Give the extent of all uninfected red blood cells.
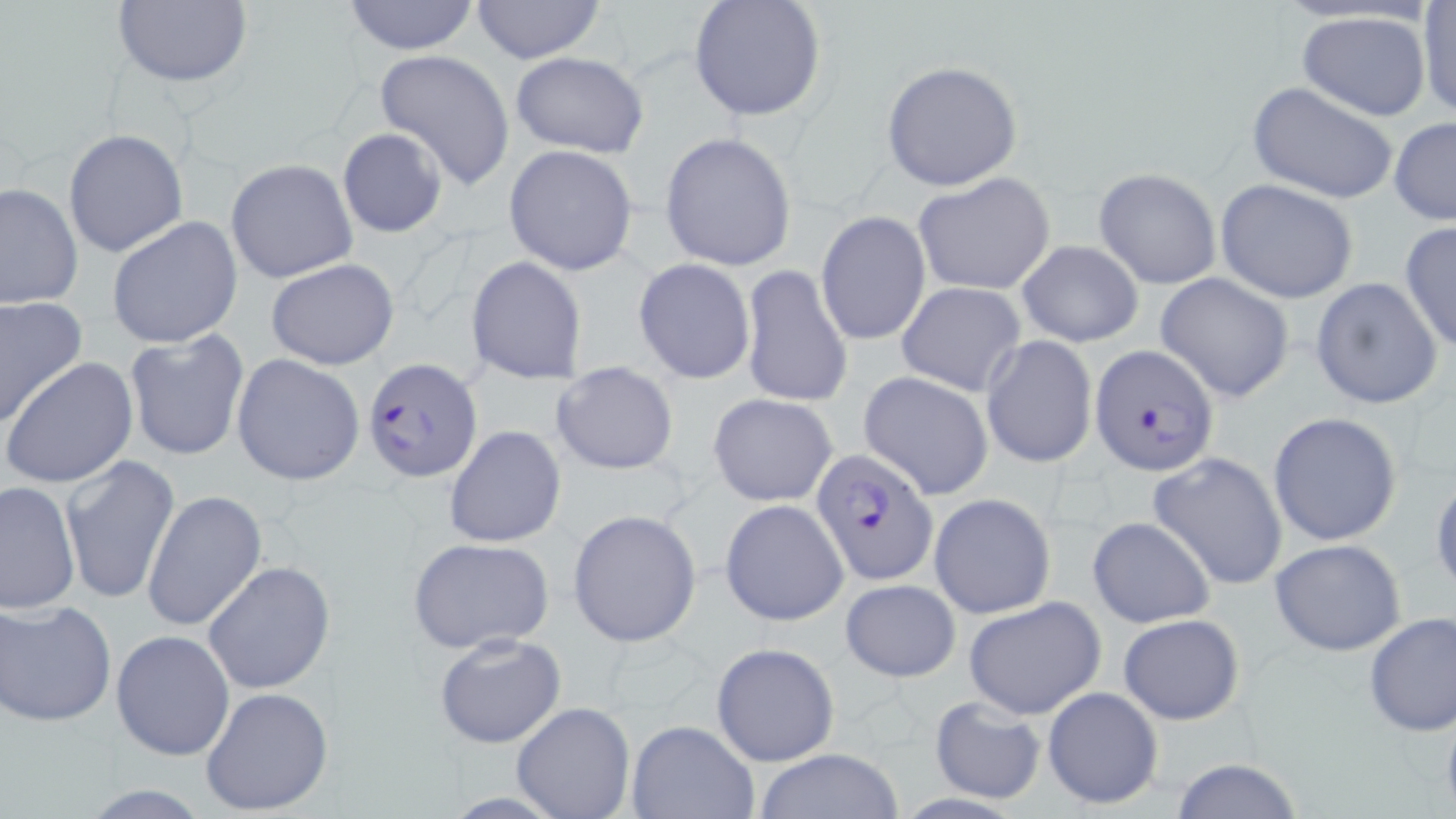
Approximate bounding boxes as (x1, y1, x2, y2) in pixels.
Uninfected red blood cells: (110, 0, 252, 91), (340, 0, 481, 55), (468, 0, 606, 65), (688, 0, 826, 123), (1416, 2, 1455, 120), (1297, 10, 1433, 121), (374, 48, 515, 191), (508, 52, 649, 159), (880, 60, 1026, 191), (1246, 83, 1398, 203), (1388, 117, 1456, 226), (336, 127, 449, 239), (64, 128, 187, 257), (660, 132, 799, 270), (504, 145, 638, 275), (226, 158, 357, 283), (1093, 166, 1222, 289), (913, 172, 1056, 297), (0, 179, 82, 309), (1215, 179, 1358, 304), (816, 210, 931, 346), (106, 216, 243, 349), (1398, 221, 1456, 355), (1016, 240, 1144, 348), (467, 256, 588, 385), (266, 258, 400, 370), (634, 258, 755, 385), (740, 265, 852, 408), (1156, 272, 1296, 403), (1310, 278, 1444, 409), (895, 281, 1027, 396), (0, 295, 89, 427), (125, 328, 249, 461), (981, 335, 1098, 470), (231, 354, 365, 486), (4, 356, 139, 489), (553, 361, 679, 475), (859, 372, 994, 500), (707, 393, 838, 508), (1268, 412, 1404, 546), (445, 424, 567, 548), (1147, 451, 1288, 590), (61, 454, 180, 606), (1430, 469, 1456, 598), (0, 479, 81, 616), (143, 489, 268, 632), (929, 492, 1056, 619), (721, 498, 848, 628), (568, 509, 701, 649), (1087, 515, 1216, 629), (407, 536, 555, 655), (1269, 537, 1407, 656), (202, 561, 335, 694), (839, 579, 962, 680), (962, 597, 1106, 719), (1, 598, 117, 727), (1362, 612, 1456, 737), (1117, 613, 1245, 725), (111, 629, 235, 760), (432, 630, 568, 748), (710, 641, 840, 768), (1041, 685, 1165, 812), (200, 686, 334, 816), (928, 695, 1049, 805), (513, 702, 635, 818), (627, 718, 760, 818), (752, 748, 903, 819), (1166, 756, 1308, 819).

slide_level_diagnosis: Plasmodium falciparum
preparation: thin blood film
stain: May-Grünwald-Giemsa
field_of_view: one of a larger specimen
magnification: 1000x
image_size: 1456×819 pixels
modality: optical microscopy
plasmodium_falciparum_infected_red_blood_cell_locations: 'approximate bounding boxes as (x1, y1, x2, y2) in pixels: (1091, 346, 1219, 475), (363, 357, 483, 481), (812, 450, 939, 584)'